State which parasite is depicted.
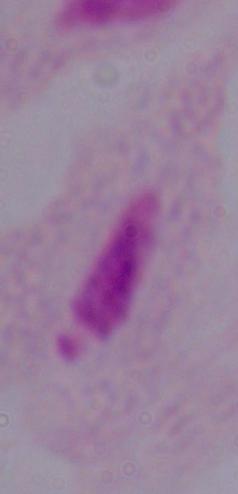
This is a trichomonad.

modality: photomicrograph
magnification: 1000x